Report the malaria status of this cell.
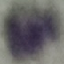

Uninfected.

Thin blood smear. Cell patch, automatically extracted from a larger field of view and resized to 64 × 64 pixels. Photographed with a smartphone camera at the microscope eyepiece. Giemsa-stained preparation.